Identify the parasite.
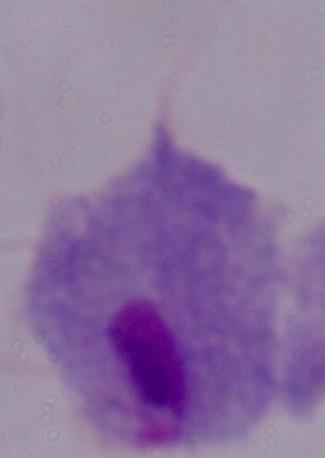
This is a trichomonad.

Micrograph. 1000x magnification.